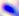
magnification = 400x
modality = photomicrograph
identification = Toxoplasma gondii